Locate every Plasmodium parasite.
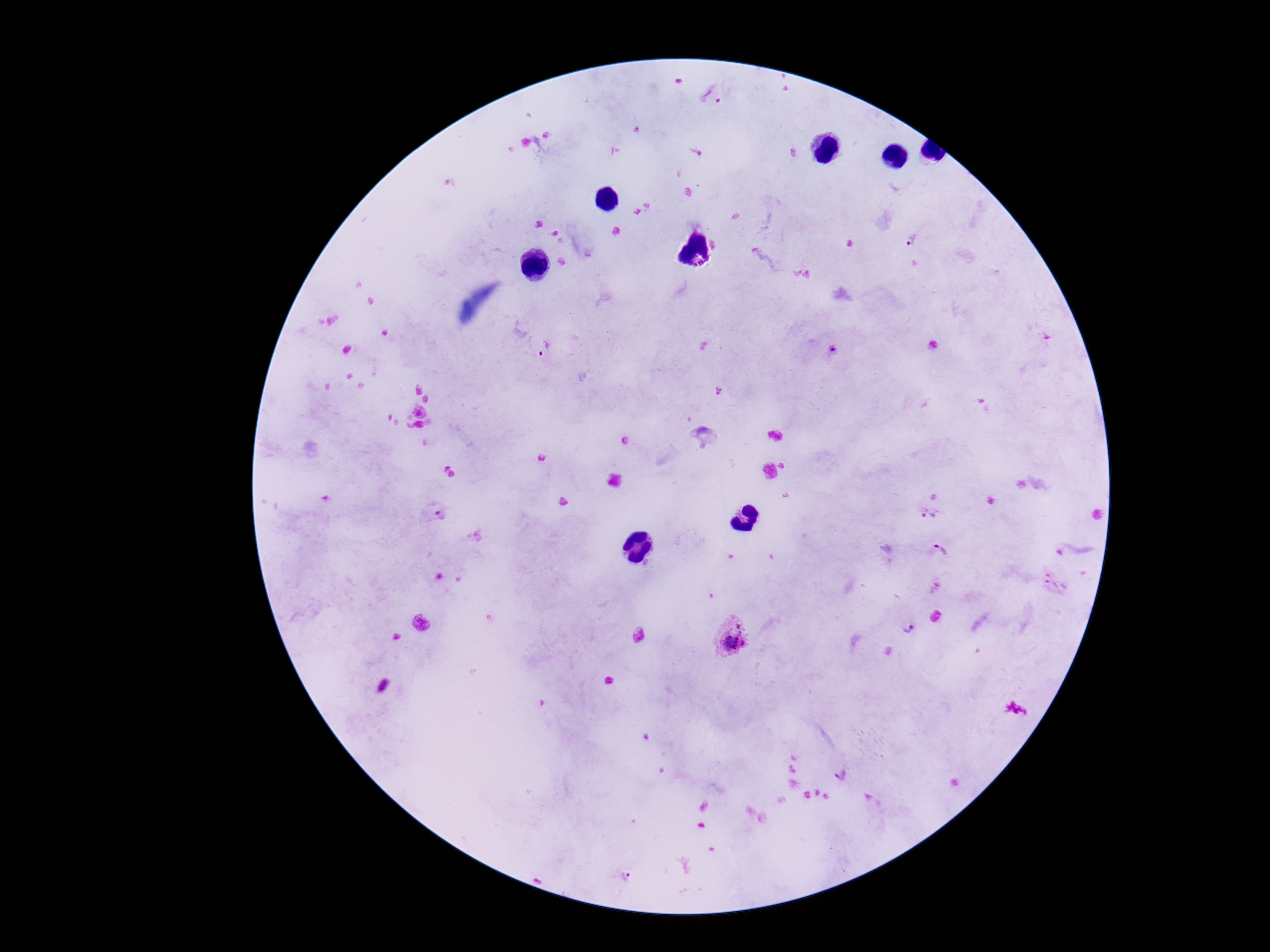

Approximate object centers, in pixels from the top-left corner.
Plasmodium parasites: (x=713, y=97), (x=912, y=241), (x=544, y=348), (x=435, y=514), (x=930, y=515), (x=940, y=551), (x=1055, y=583), (x=906, y=626), (x=732, y=637), (x=840, y=774), (x=625, y=877).

Summary:
  - Field of view: single
  - Preparation: thick peripheral-blood smear
  - Image size: 1270×952 pixels
  - Patient malaria status: positive
  - Capture: smartphone camera through the microscope eyepiece
  - Magnification: 100x
  - Stain: Giemsa